Classify this cell by malaria status.
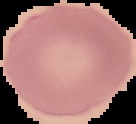

It is uninfected.

Image is 136×124 pixels. From a thin blood smear. Cell region segmented out of the field of view; the surrounding area is masked to black.